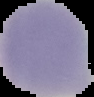
malaria status = uninfected
image type = cell region segmented out of the field of view; surrounding area masked to black
image size = 94×97 pixels
preparation = thin blood smear